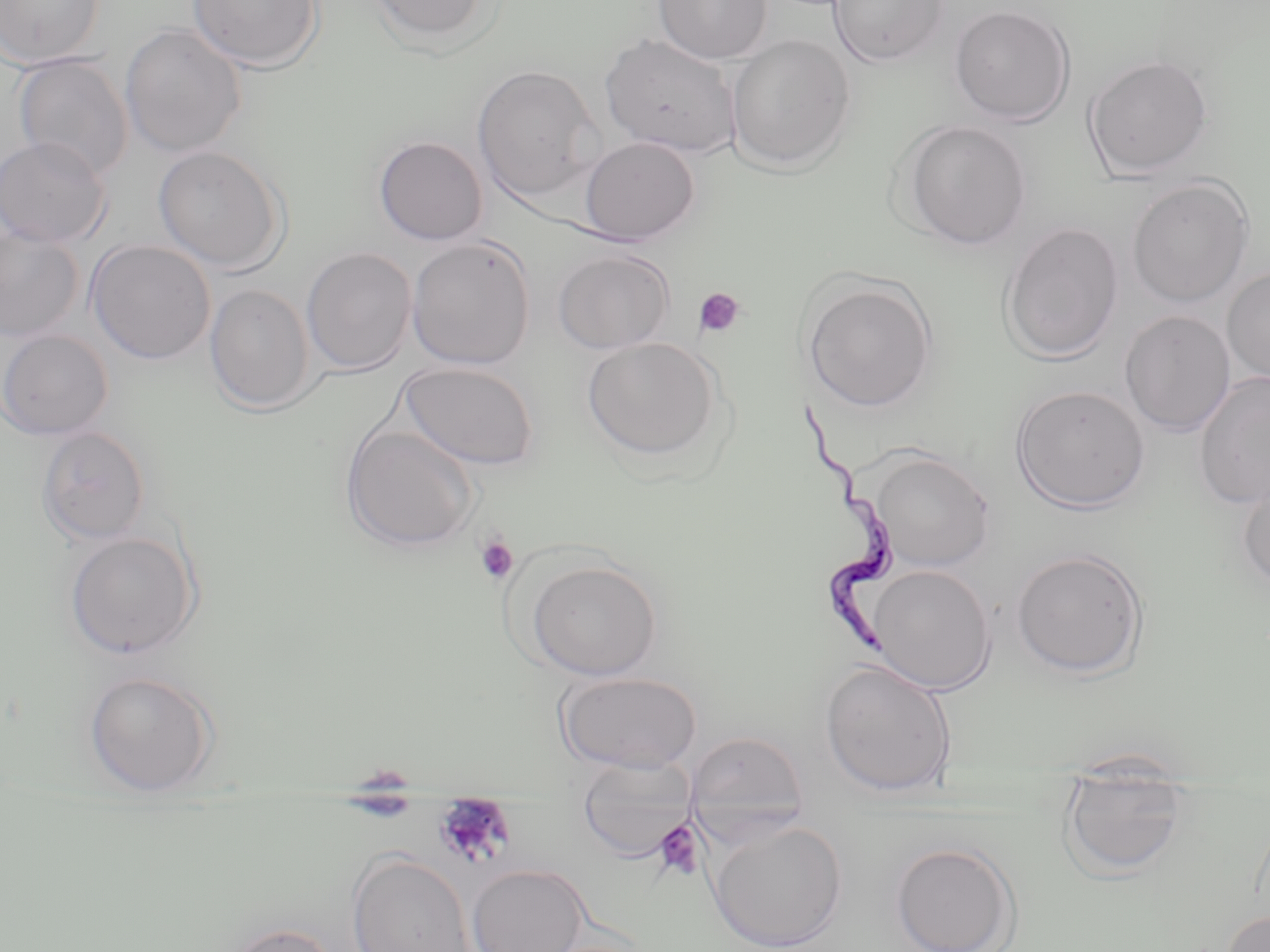

Trypanosoma brucei locations = approximate bounding boxes as named x1/y1/x2/y2 corners in pixels: (x1=789, y1=401, x2=898, y2=657)
slide-level diagnosis = Trypanosoma brucei
preparation = thin blood film
field of view = one of a larger specimen
stain = May-Grünwald-Giemsa
magnification = 1000x
image size = 1270×952 pixels
modality = optical microscopy
platelet locations = approximate bounding boxes as named x1/y1/x2/y2 corners in pixels: (x1=693, y1=287, x2=746, y2=339), (x1=473, y1=536, x2=519, y2=586), (x1=337, y1=766, x2=418, y2=824), (x1=433, y1=797, x2=516, y2=869), (x1=652, y1=820, x2=705, y2=881)
uninfected red blood cell locations = approximate bounding boxes as named x1/y1/x2/y2 corners in pixels: (x1=0, y1=0, x2=105, y2=69), (x1=186, y1=0, x2=324, y2=71), (x1=367, y1=0, x2=496, y2=47), (x1=654, y1=0, x2=772, y2=64), (x1=827, y1=0, x2=950, y2=67), (x1=949, y1=4, x2=1076, y2=126), (x1=119, y1=23, x2=247, y2=158), (x1=599, y1=32, x2=743, y2=158), (x1=726, y1=34, x2=856, y2=173), (x1=1083, y1=53, x2=1214, y2=178), (x1=13, y1=54, x2=133, y2=181), (x1=472, y1=64, x2=603, y2=203), (x1=898, y1=119, x2=1033, y2=250), (x1=373, y1=135, x2=488, y2=246), (x1=0, y1=136, x2=111, y2=248), (x1=579, y1=136, x2=700, y2=245), (x1=152, y1=145, x2=288, y2=273), (x1=1126, y1=177, x2=1255, y2=308), (x1=999, y1=222, x2=1124, y2=363), (x1=0, y1=225, x2=85, y2=343), (x1=406, y1=235, x2=537, y2=370), (x1=86, y1=239, x2=216, y2=365), (x1=300, y1=246, x2=418, y2=375), (x1=553, y1=249, x2=676, y2=354), (x1=1221, y1=267, x2=1270, y2=386), (x1=800, y1=275, x2=938, y2=413), (x1=204, y1=284, x2=315, y2=413), (x1=1118, y1=310, x2=1236, y2=436), (x1=0, y1=330, x2=114, y2=440), (x1=581, y1=337, x2=723, y2=464), (x1=399, y1=361, x2=541, y2=471), (x1=1194, y1=371, x2=1270, y2=511), (x1=1011, y1=384, x2=1151, y2=513), (x1=340, y1=423, x2=480, y2=553), (x1=35, y1=425, x2=152, y2=545), (x1=867, y1=449, x2=995, y2=572), (x1=1237, y1=472, x2=1270, y2=591), (x1=64, y1=530, x2=202, y2=659), (x1=1010, y1=547, x2=1149, y2=679), (x1=522, y1=557, x2=664, y2=681), (x1=867, y1=564, x2=997, y2=694), (x1=819, y1=659, x2=958, y2=799), (x1=82, y1=670, x2=218, y2=794), (x1=554, y1=670, x2=703, y2=773), (x1=684, y1=730, x2=811, y2=844), (x1=573, y1=761, x2=699, y2=860), (x1=1057, y1=765, x2=1192, y2=881), (x1=706, y1=817, x2=848, y2=952), (x1=890, y1=841, x2=1021, y2=952), (x1=346, y1=851, x2=475, y2=952), (x1=467, y1=864, x2=590, y2=952), (x1=1220, y1=908, x2=1270, y2=952), (x1=214, y1=921, x2=345, y2=952)